Locate every Plasmodium parasite.
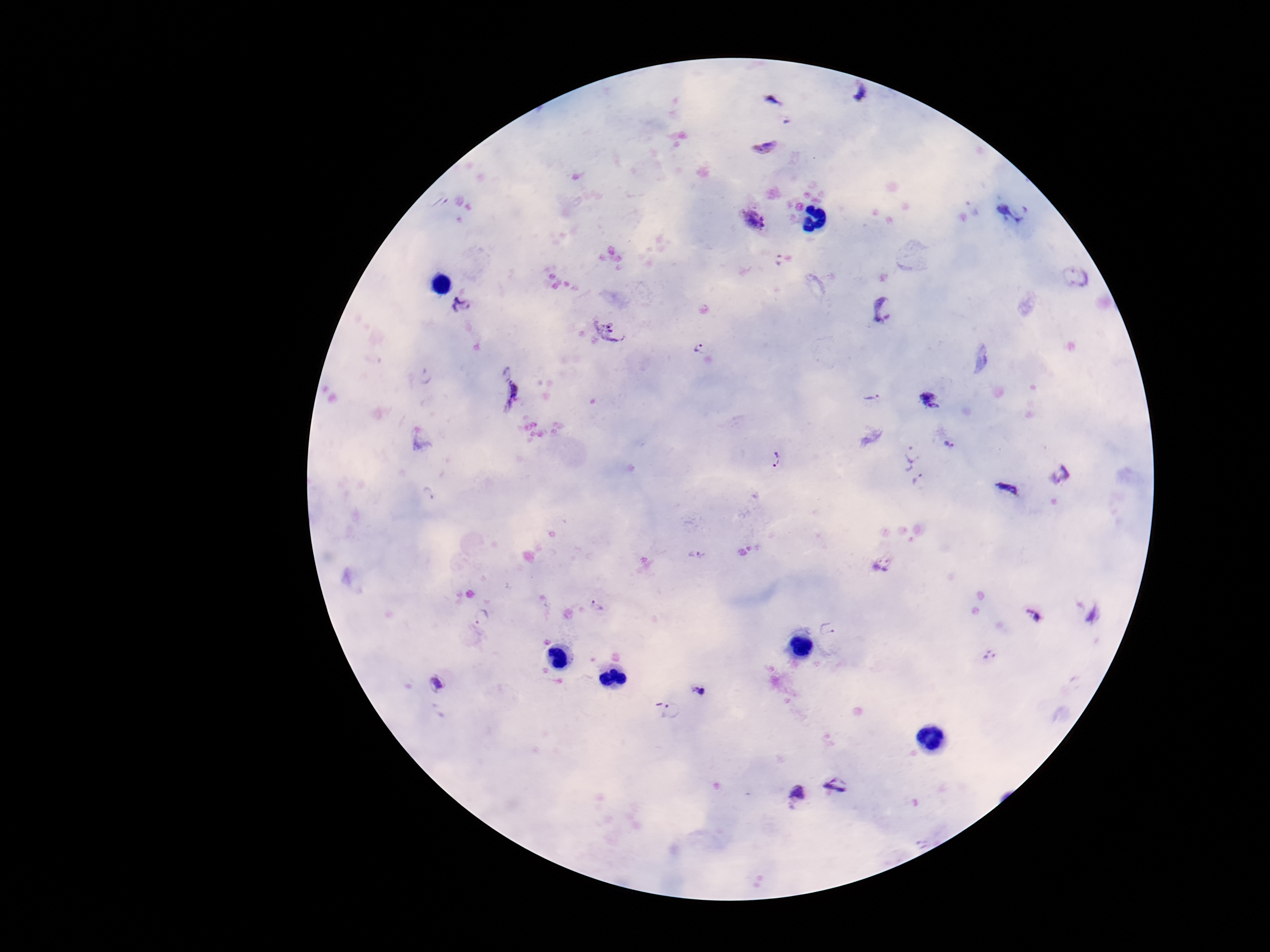

Approximate centers as {x, y} in pixels.
Plasmodium parasites: {863, 94}, {1012, 212}, {753, 220}, {779, 259}, {1078, 279}, {462, 305}, {883, 309}, {608, 331}, {699, 349}, {428, 377}, {512, 396}, {871, 397}, {930, 400}, {948, 445}, {911, 453}, {776, 461}, {1060, 475}, {919, 483}, {1009, 488}, {430, 493}, {696, 554}, {881, 560}, {597, 606}, {1034, 615}, {481, 618}, {828, 628}, {990, 656}, {438, 683}, {699, 691}, {671, 711}, {838, 786}, {793, 795}.

Thick peripheral-blood smear. Patient malaria status: positive. One field from this slide. 100x magnification. Photographed through the microscope eyepiece with a smartphone camera. Image is 1270×952 pixels. Giemsa stain.